Name the parasite shown.
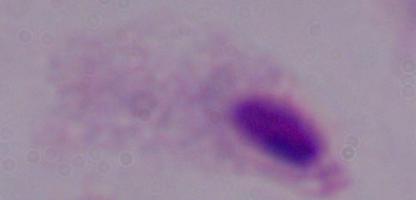
This is a trichomonad.

magnification = 1000x
modality = photomicrograph